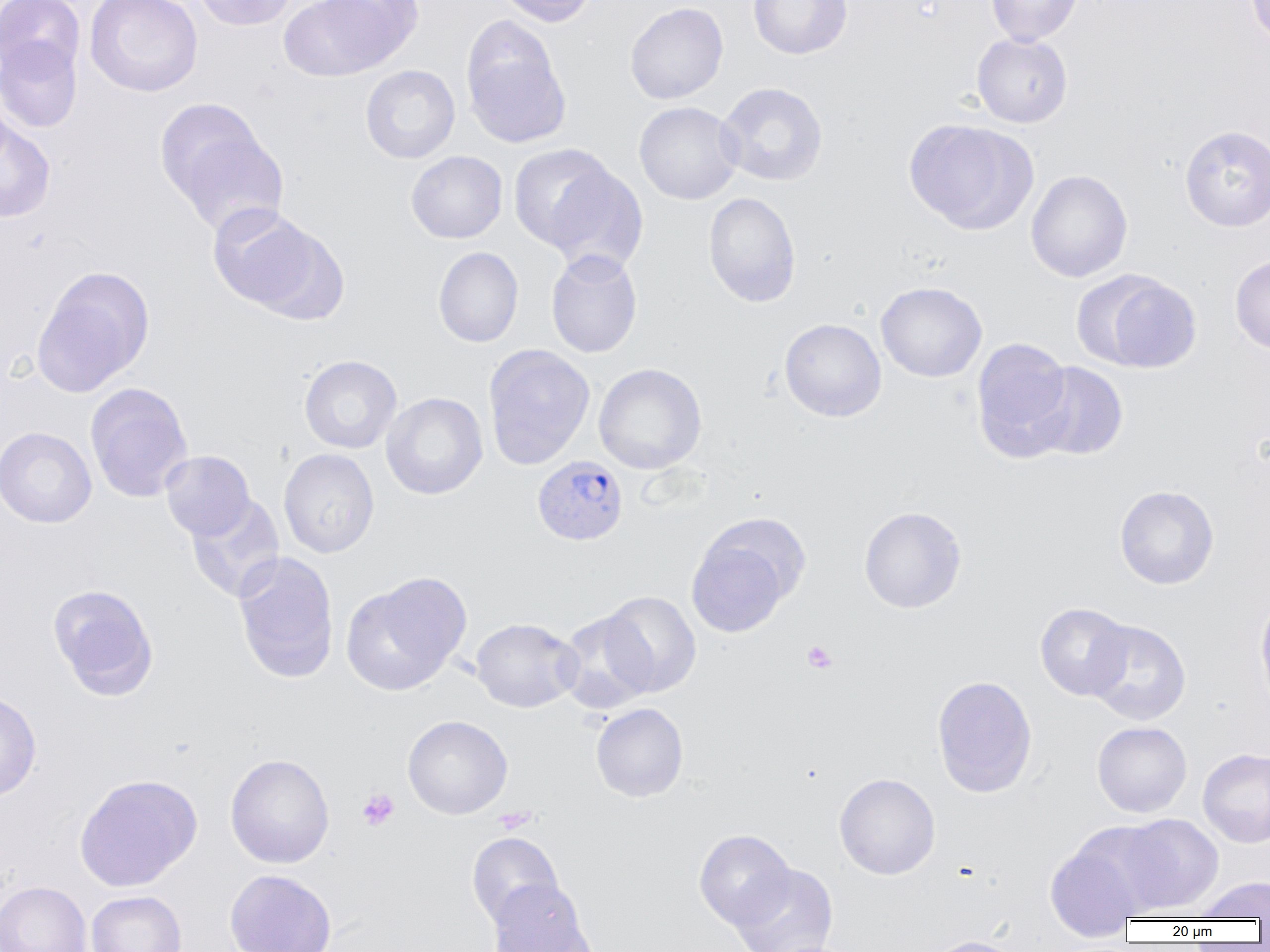
Summary:
  - Coordinate format: approximate bounding boxes as (x1,y1)-(x2,y2) corner pairs in pixels
  - Platelet locations: (801,640)-(838,674), (357,788)-(400,831), (495,806)-(536,834)
  - Plasmodium vivax-infected red blood cell locations: (532,454)-(628,546)
  - Uninfected red blood cell locations: (0,0)-(85,78), (84,0)-(203,97), (193,0)-(297,30), (279,0)-(398,81), (494,0)-(598,26), (748,0)-(852,59), (986,0)-(1083,46), (1244,0)-(1270,50), (625,2)-(728,104), (461,18)-(571,148), (972,33)-(1073,128), (0,36)-(83,134), (360,65)-(460,163), (716,82)-(828,186), (0,87)-(15,175), (634,101)-(743,205), (166,117)-(288,235), (904,118)-(1037,234), (0,119)-(56,223), (1179,124)-(1270,231), (509,144)-(617,253), (406,150)-(508,243), (543,163)-(649,275), (1025,169)-(1133,282), (703,192)-(801,307), (208,204)-(343,321), (433,246)-(524,347), (545,249)-(643,358), (1230,254)-(1270,354), (32,267)-(154,396), (1076,270)-(1202,373), (876,281)-(986,382), (779,318)-(886,421), (971,337)-(1075,460), (483,344)-(595,470), (299,354)-(402,454), (1028,361)-(1129,460), (594,363)-(707,474), (85,382)-(193,503), (381,392)-(488,499), (0,426)-(97,527), (279,448)-(380,558), (160,450)-(255,540), (1114,485)-(1219,589), (186,494)-(285,602), (859,505)-(968,613), (685,515)-(806,638), (233,552)-(339,683), (341,573)-(471,695), (47,584)-(159,700), (600,591)-(702,697), (1255,591)-(1270,714), (1035,602)-(1134,700), (557,611)-(656,714), (470,618)-(581,712), (1085,619)-(1191,725), (931,674)-(1038,798), (0,690)-(42,801), (590,702)-(689,802), (402,715)-(512,819), (1092,721)-(1192,817), (1198,748)-(1270,848), (225,753)-(335,868), (834,772)-(940,880), (74,773)-(202,892), (1115,813)-(1224,915), (693,829)-(796,929), (466,832)-(564,929), (1044,837)-(1147,940), (731,862)-(838,951), (225,869)-(337,951), (1193,876)-(1270,921), (487,880)-(595,952), (0,881)-(92,952), (85,890)-(186,952), (924,935)-(1025,952)
  - Slide-level diagnosis: Plasmodium vivax
  - Field of view: single
  - Preparation: thin blood smear
  - Modality: optical microscopy
  - Magnification: 1000x
  - Image size: 1270×952 pixels